Identify the preparation type.
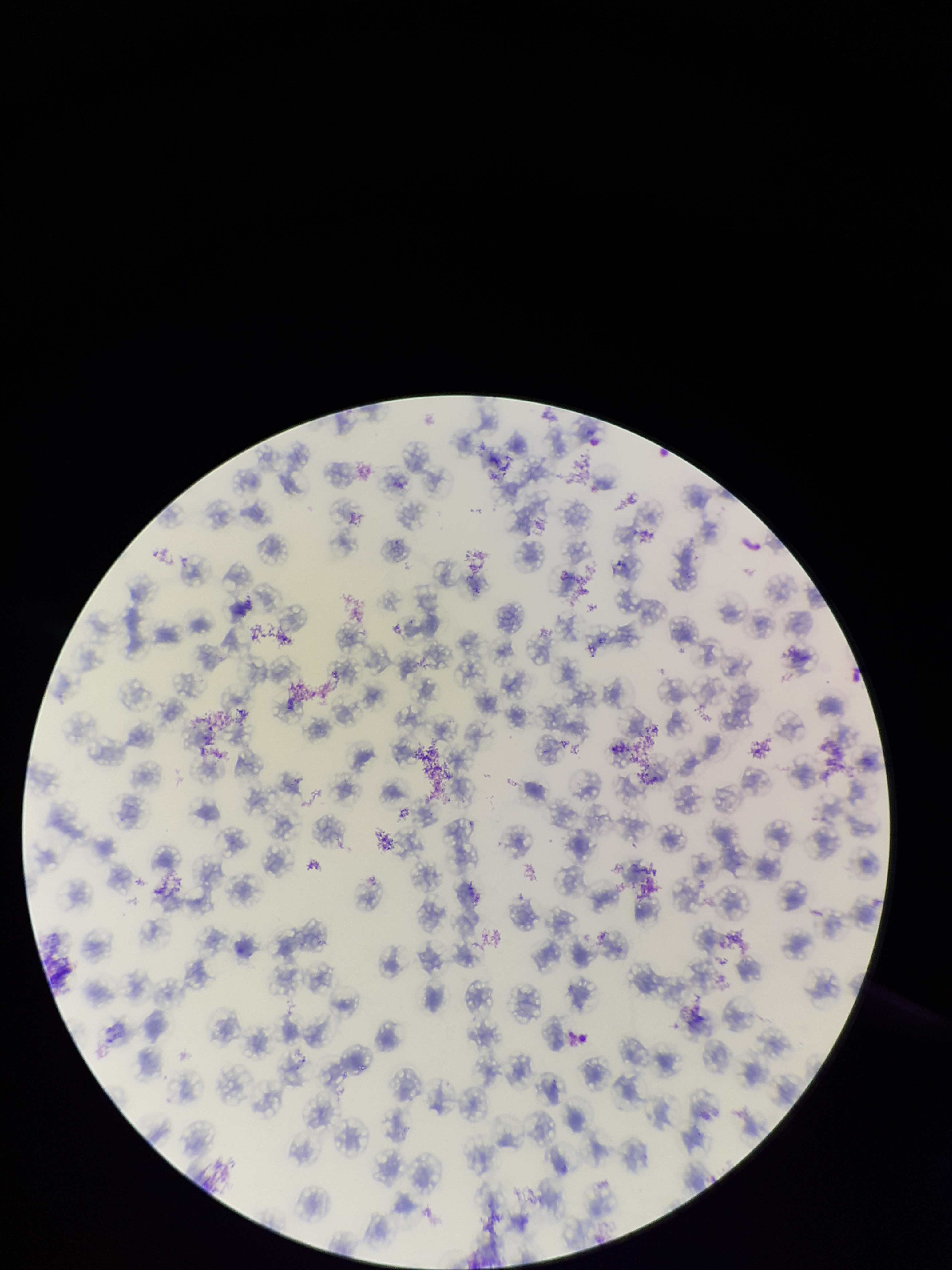

A thin smear.

Summary:
  - Red blood cell count: 113
  - Stain: Giemsa
  - Field of view: single
  - Species reported for this patient: Plasmodium falciparum
  - Image size: 952×1270 pixels
  - Parasitized red blood cells: none identified
  - Capture: smartphone photograph through the microscope eyepiece
  - Parasitized red blood cell count: 0
  - Patient malaria status: infected